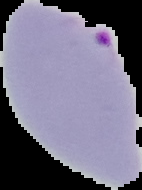 From a thin blood smear. Result: Plasmodium parasites identified. Image is 142×190 pixels. Segmented cell region on a black background.